Assess the morphology of the red blood cells.
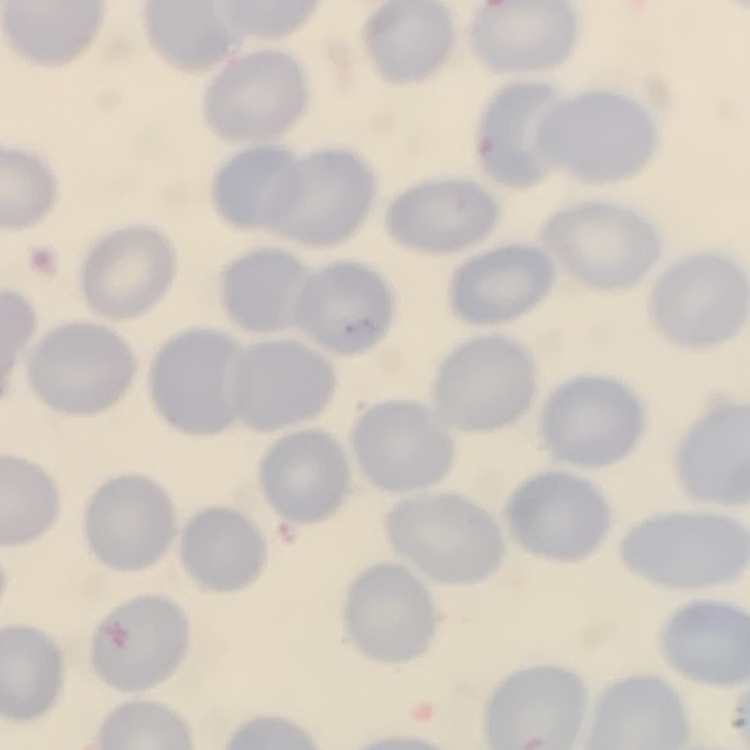

No rouleaux formation.

Summary:
  - Preparation: thin peripheral smear
  - Stain: Field's or Giemsa
  - Image type: one tile cut from a larger photomicrograph